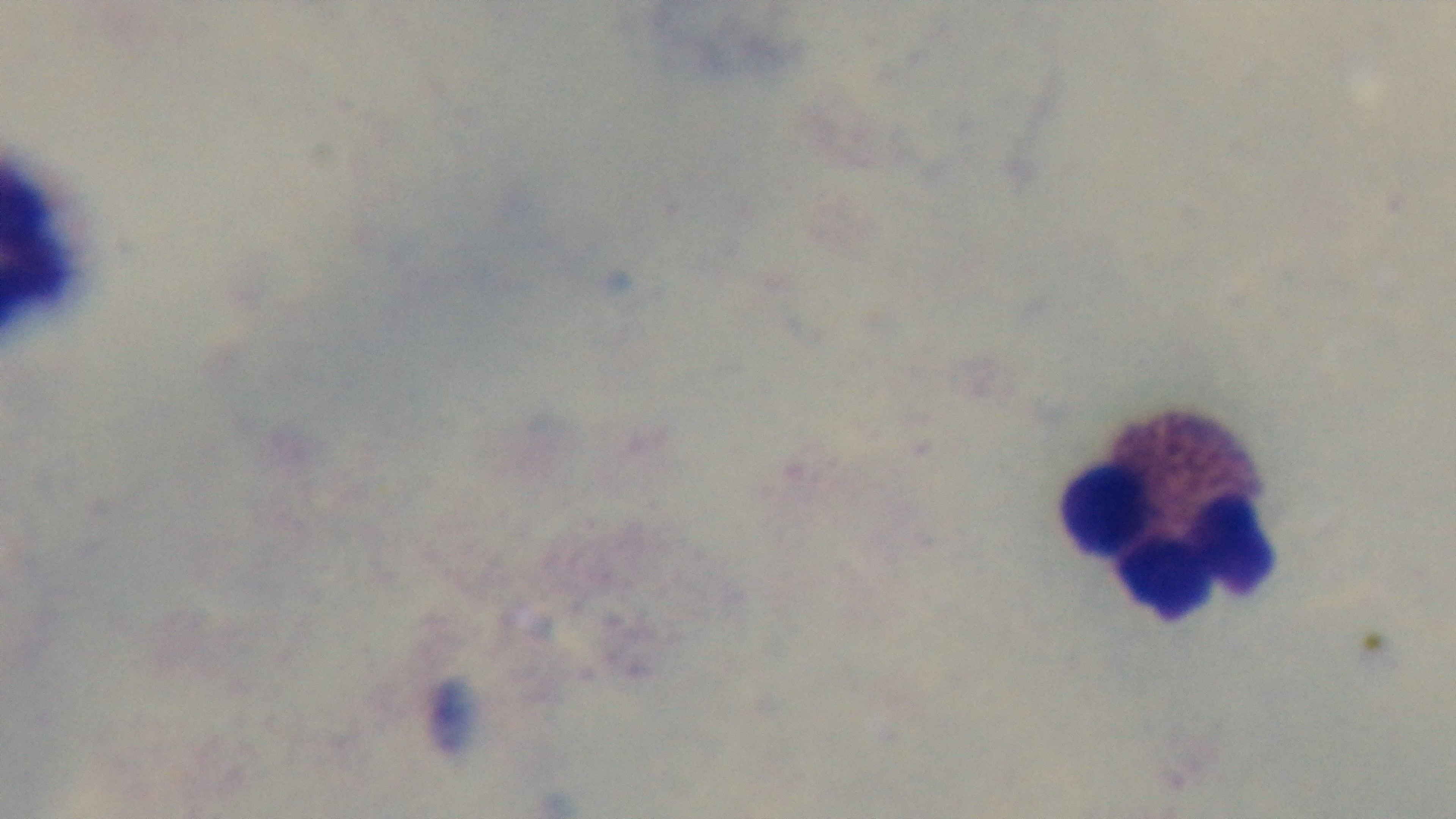

stain = Giemsa
capture = mounted 4K digital camera
modality = light microscopy
field of view = one from the slide
malaria status = uninfected
preparation = thick
objective = 100x oil immersion